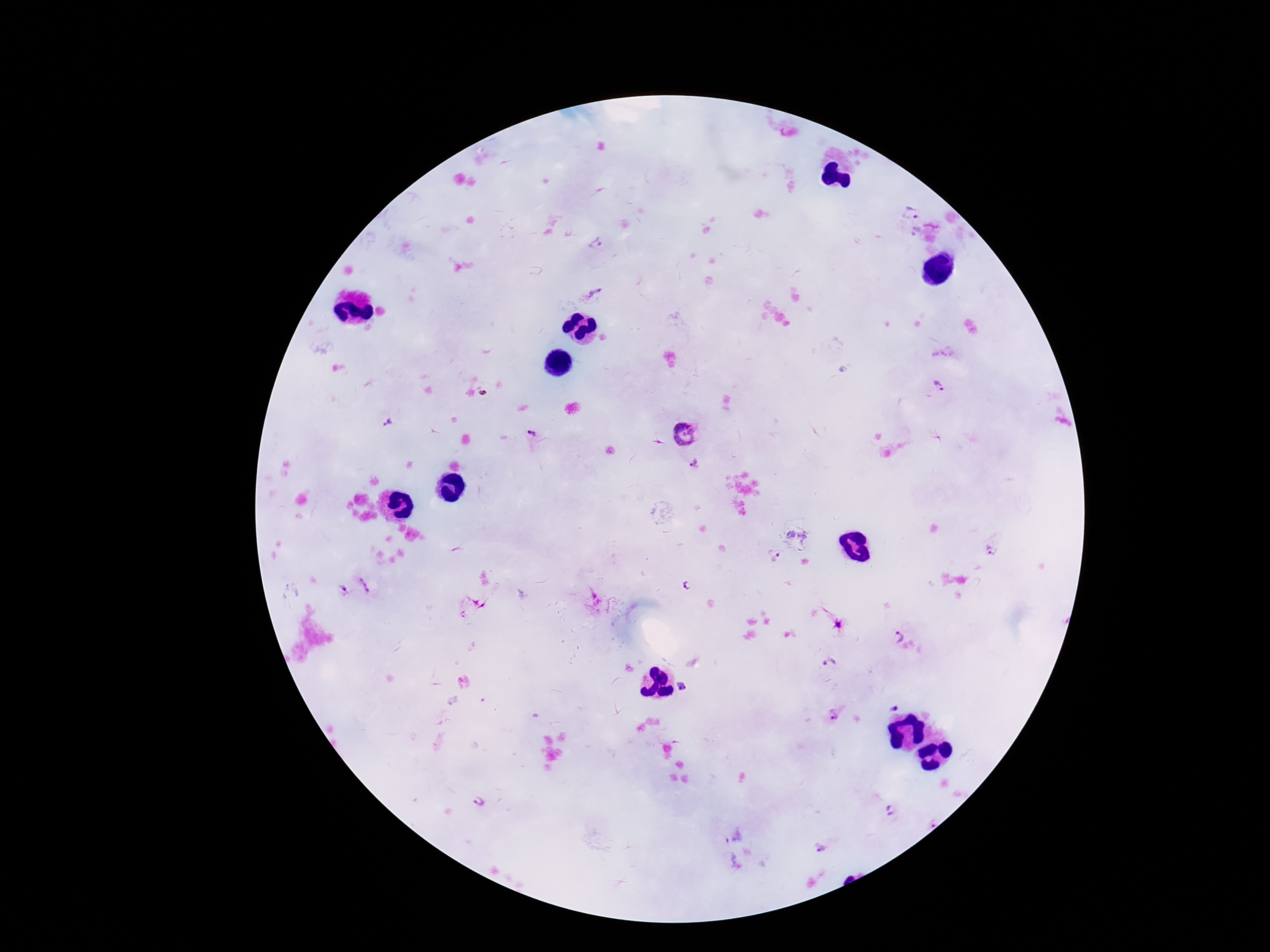
Approximate centers as (x, y) in pixels.
Summary:
  - Plasmodium parasite locations: (909, 212), (916, 233), (595, 244), (594, 292), (938, 386), (388, 424), (531, 432), (684, 434), (695, 465), (992, 551), (775, 556), (364, 585), (685, 586), (343, 588), (898, 638), (829, 664), (681, 686), (894, 707), (833, 717), (478, 802), (892, 811), (821, 850)
  - Field of view: single
  - Patient malaria status: positive
  - Magnification: 100x
  - Capture: smartphone camera through the microscope eyepiece
  - Preparation: thick blood film
  - Stain: Giemsa
  - Image size: 1270×952 pixels